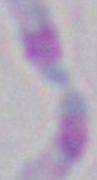

modality: photomicrograph
identification: Toxoplasma gondii
magnification: 1000x